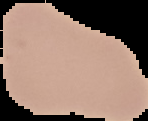
Summary:
  - Image type: segmented cell region on a black background
  - Malaria status: uninfected
  - Image size: 148×121 pixels
  - Preparation: thin blood film